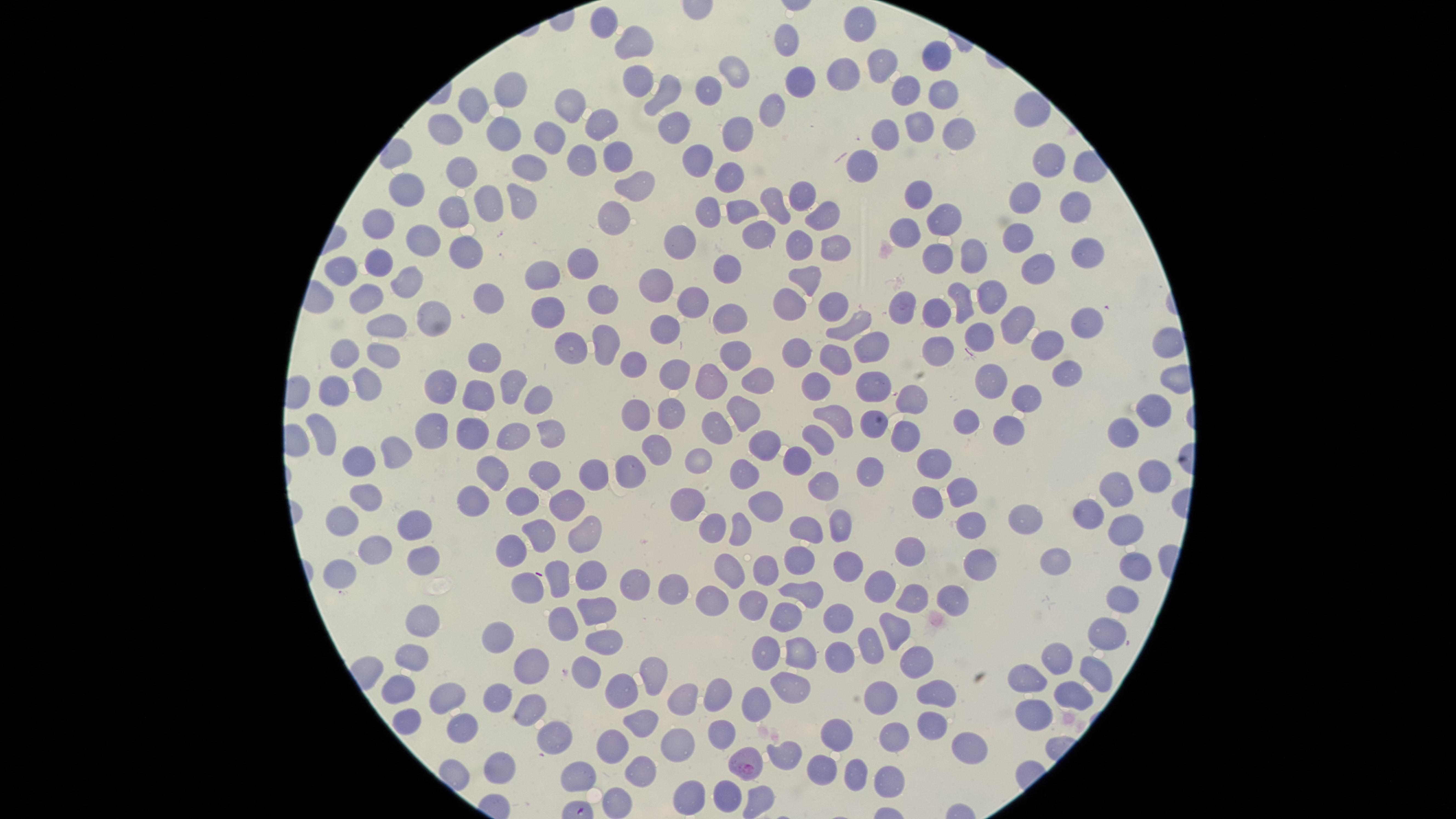

Approximate marker points as {x, y} in pixels.
Summary:
  - Uninfected red blood cells: {607, 17}, {861, 23}, {635, 43}, {782, 46}, {937, 54}, {883, 66}, {735, 69}, {839, 73}, {638, 79}, {796, 81}, {907, 87}, {942, 89}, {666, 90}, {709, 90}, {510, 92}, {472, 102}, {566, 103}, {771, 111}, {446, 124}, {917, 126}, {600, 127}, {507, 128}, {672, 129}, {883, 129}, {956, 132}, {545, 134}, {737, 137}, {616, 153}, {697, 153}, {1045, 153}, {580, 154}, {863, 160}, {528, 164}, {459, 166}, {733, 178}, {640, 181}, {409, 184}, {801, 191}, {915, 194}, {1022, 194}, {517, 196}, {483, 198}, {774, 201}, {1073, 203}, {743, 206}, {444, 210}, {707, 213}, {820, 214}, {939, 217}, {619, 220}, {373, 222}, {762, 229}, {901, 230}, {1021, 233}, {422, 238}, {680, 242}, {795, 247}, {831, 247}, {465, 249}, {1088, 249}, {977, 251}, {376, 257}, {940, 259}, {1038, 259}, {577, 263}, {541, 270}, {726, 270}, {805, 272}, {339, 273}, {402, 277}, {661, 281}, {495, 291}, {990, 292}, {368, 295}, {600, 300}, {960, 300}, {794, 301}, {829, 301}, {903, 304}, {542, 309}, {692, 309}, {943, 313}, {731, 317}, {433, 320}, {852, 323}, {1017, 323}, {1085, 323}, {387, 325}, {665, 329}, {979, 334}, {935, 343}, {865, 344}, {1049, 344}, {606, 345}, {344, 349}, {735, 350}, {570, 353}, {802, 355}, {385, 356}, {481, 358}, {835, 358}, {634, 360}, {1061, 372}, {674, 376}, {989, 377}, {370, 378}, {714, 379}, {755, 381}, {513, 382}, {819, 385}, {872, 386}, {480, 388}, {439, 389}, {322, 393}, {911, 394}, {1027, 396}, {539, 401}, {1148, 407}, {636, 410}, {742, 410}, {673, 412}, {838, 415}, {966, 417}, {714, 419}, {996, 422}, {428, 425}, {864, 425}, {323, 428}, {471, 430}, {1119, 430}, {513, 432}, {547, 432}, {909, 435}, {817, 440}, {761, 447}, {387, 449}, {651, 450}, {798, 453}, {933, 458}, {699, 459}, {360, 460}, {598, 470}, {492, 471}, {633, 471}, {868, 471}, {547, 474}, {744, 474}, {1151, 476}, {818, 481}, {1116, 486}, {366, 492}, {469, 492}, {958, 492}, {519, 495}, {925, 498}, {686, 499}, {561, 503}, {759, 506}, {1089, 509}, {343, 518}, {1029, 518}, {418, 521}, {834, 523}, {966, 523}, {714, 524}, {809, 525}, {543, 531}, {735, 531}, {580, 534}, {1122, 534}, {376, 547}, {512, 550}, {914, 552}, {420, 558}, {800, 561}, {976, 564}, {1053, 564}, {852, 568}, {344, 569}, {765, 569}, {723, 571}, {591, 572}, {1131, 572}, {558, 577}, {526, 583}, {635, 583}, {879, 584}, {678, 587}, {807, 590}, {911, 595}, {714, 598}, {952, 598}, {1119, 598}, {749, 599}, {596, 607}, {792, 610}, {834, 619}, {420, 625}, {561, 625}, {893, 626}, {1105, 633}, {496, 640}, {603, 641}, {869, 642}, {796, 646}, {1057, 651}, {838, 654}, {762, 655}, {414, 656}, {534, 658}, {921, 666}, {588, 668}, {1033, 676}, {1094, 676}, {651, 682}, {787, 682}, {618, 686}, {398, 690}, {718, 691}, {934, 693}, {687, 694}, {1070, 695}, {446, 696}, {883, 696}, {501, 697}, {758, 703}, {527, 708}, {1034, 709}, {645, 716}, {409, 722}, {931, 722}, {460, 728}, {556, 728}, {717, 733}, {897, 734}, {832, 736}, {612, 743}, {676, 743}, {968, 745}, {782, 752}, {820, 761}, {503, 766}, {636, 768}, {575, 773}, {854, 773}, {888, 778}, {690, 788}, {727, 792}, {757, 794}, {619, 798}
  - Parasitized red blood cells: {748, 762}
  - Species: Plasmodium falciparum
  - Field of view: single
  - Capture: smartphone photograph through the microscope eyepiece
  - Preparation: thin blood film
  - Presence: malaria parasites seen
  - Stain: Giemsa
  - Visible region: circular
  - Image size: 1456×819 pixels